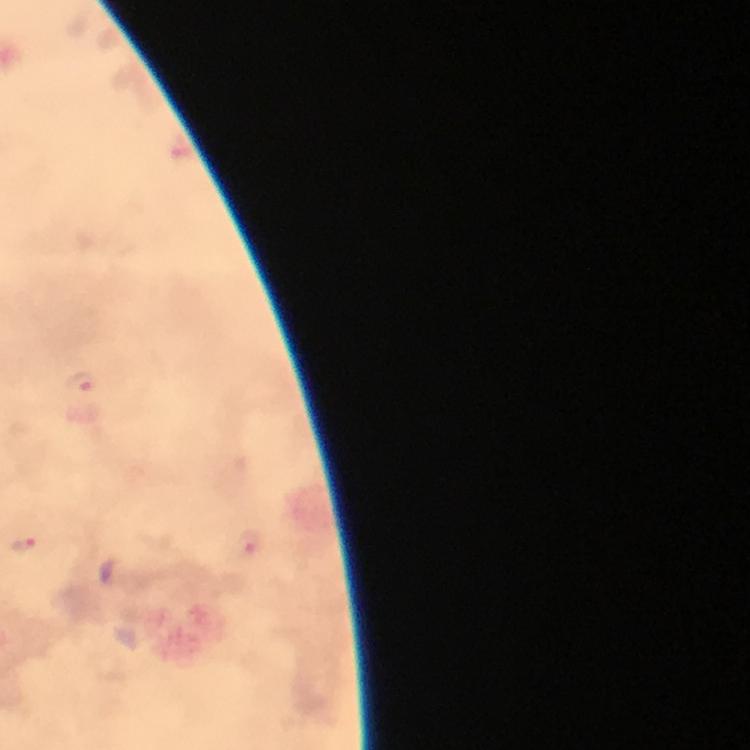

Approximate centers as {x, y} in pixels.
Summary:
  - Malaria parasite locations: {84, 384}, {22, 545}, {251, 547}
  - Preparation: thick blood film
  - Magnification: 100x
  - Capture: smartphone camera through the microscope
  - Cropped from: one field of view
  - Immersion oil: used
  - Context: from a diagnostic examination for malaria
  - Image size: 750×750 pixels
  - Stain: Giemsa